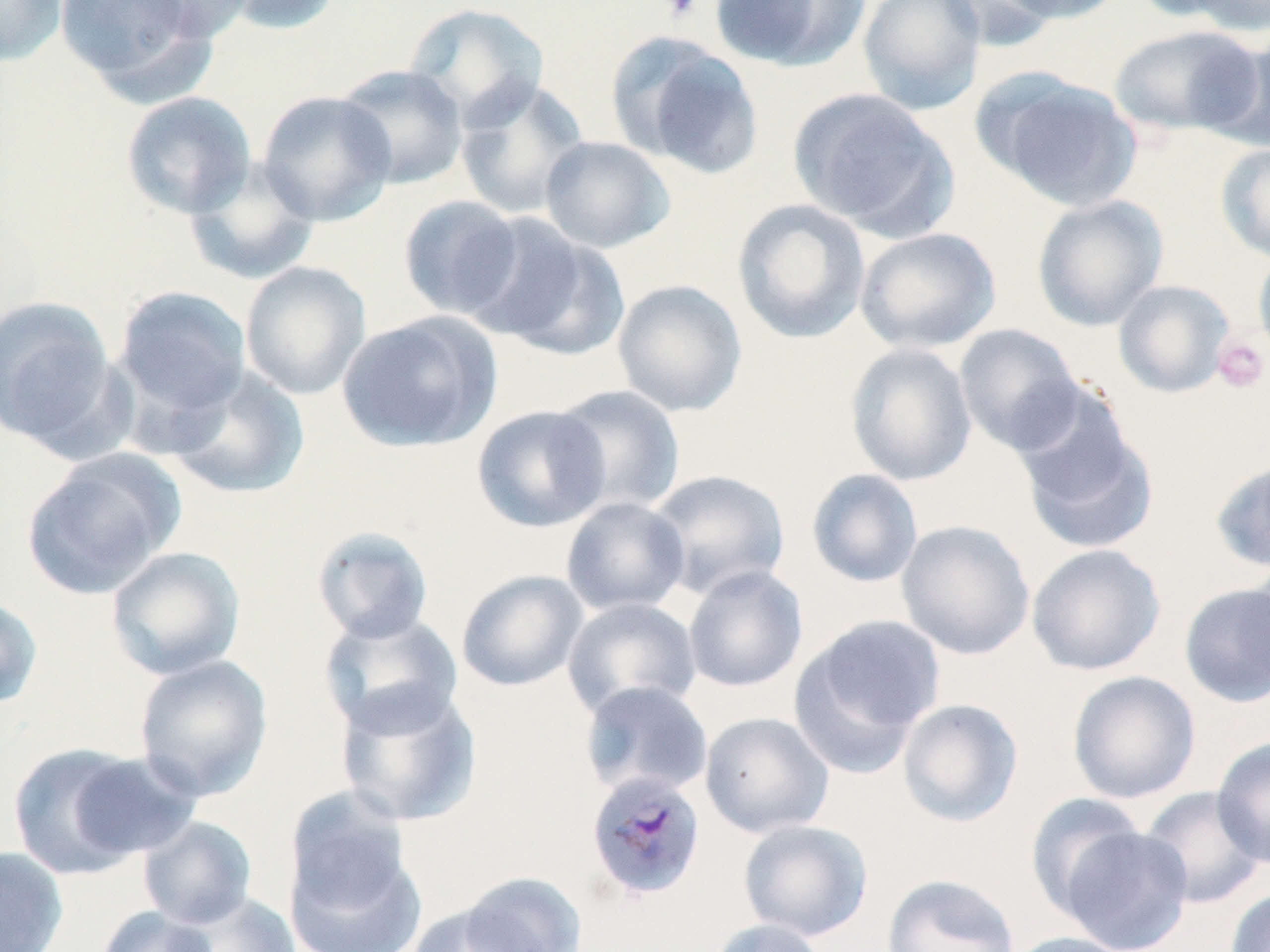 Approximate bounding boxes as (x1,y1)-(x2,y2) corner pairs in pixels. Uninfected red blood cell locations: (0,0)-(67,68), (53,0)-(213,95), (130,0)-(259,42), (219,0)-(346,36), (708,0)-(871,72), (857,0)-(988,115), (938,0)-(1063,50), (992,0)-(1130,24), (1130,0)-(1255,24), (1176,0)-(1270,35), (403,2)-(549,129), (1107,24)-(1263,139), (608,33)-(764,178), (1201,36)-(1270,150), (335,64)-(469,189), (983,73)-(1142,212), (454,77)-(590,220), (788,88)-(956,237), (121,91)-(256,219), (257,91)-(397,226), (540,136)-(675,253), (1215,142)-(1270,264), (183,157)-(320,286), (397,195)-(526,321), (1031,195)-(1168,331), (731,198)-(871,345), (472,216)-(628,360), (854,226)-(1001,354), (1253,249)-(1270,365), (239,262)-(372,401), (612,279)-(748,417), (1112,279)-(1235,399), (112,285)-(252,423), (0,296)-(119,451), (336,311)-(501,454), (953,323)-(1084,455), (844,342)-(978,486), (163,366)-(310,500), (549,384)-(686,516), (1014,402)-(1158,555), (471,404)-(611,533), (20,449)-(184,597), (1210,457)-(1270,574), (646,468)-(791,601), (806,468)-(924,588), (560,496)-(691,617), (896,519)-(1035,660), (311,525)-(435,643), (1026,543)-(1166,676), (105,546)-(246,681), (1241,558)-(1270,691), (682,564)-(809,693), (455,568)-(589,692), (1178,581)-(1270,707), (0,594)-(44,712), (562,597)-(702,719), (318,610)-(464,737), (791,615)-(945,768), (133,654)-(274,802), (1066,670)-(1201,804), (579,680)-(714,799), (335,682)-(482,828), (897,698)-(1023,828), (699,711)-(835,838), (1211,735)-(1270,870), (5,742)-(182,878), (1140,786)-(1268,910), (1026,793)-(1150,920), (138,816)-(257,929), (738,818)-(873,941), (1056,825)-(1194,951), (284,834)-(427,952), (0,845)-(69,952), (458,870)-(588,952), (881,873)-(1020,952), (1224,887)-(1270,952), (171,891)-(300,952), (404,903)-(548,952), (95,906)-(219,952), (704,918)-(832,952), (1004,931)-(1136,952). Platelet locations: (657,0)-(704,22), (1212,335)-(1268,393). Plasmodium malariae-infected red blood cell locations: (584,770)-(707,903). Slide-level diagnosis: Plasmodium malariae. Optical microscopy. 1000x magnification. One field of a larger specimen. May-Grünwald-Giemsa-stained preparation. Thin blood smear. Image is 1270×952 pixels.